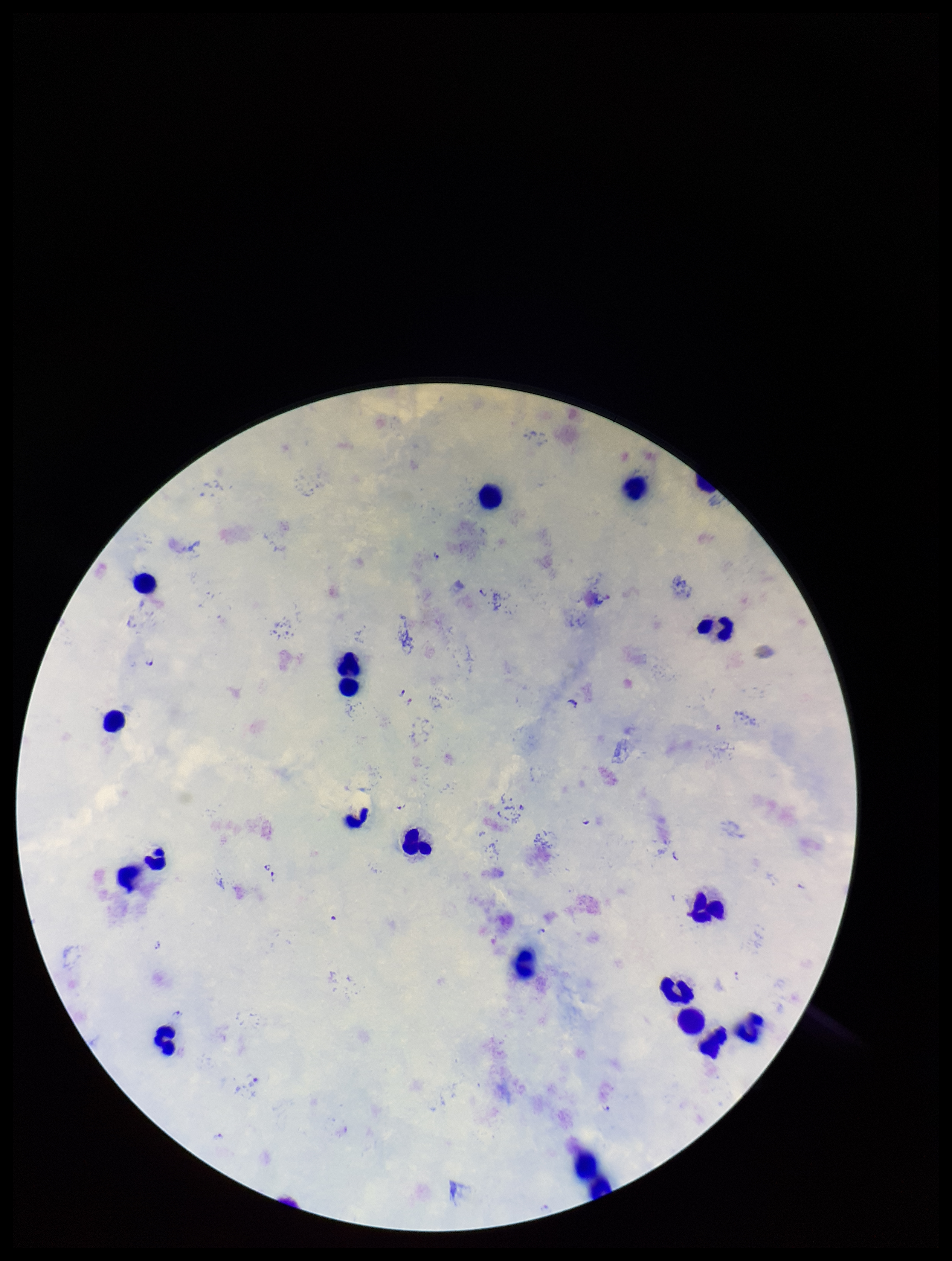

field of view = single
stain = Giemsa
image size = 952×1261 pixels
Plasmodium parasites = identified
leukocyte count = 19
parasite count = 12
patient malaria status = infected
capture = smartphone photograph through the microscope eyepiece
preparation = thick
species reported for this patient = Plasmodium falciparum